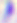
Summary:
  - Modality: photomicrograph
  - Identification: Toxoplasma gondii
  - Magnification: 400x